Identify the parasite.
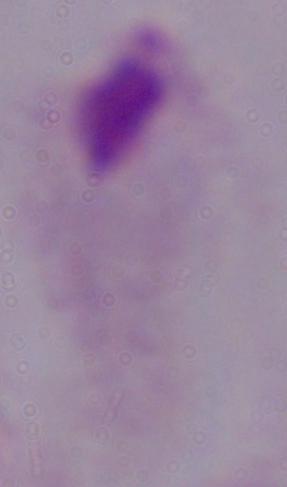

A trichomonad.

Summary:
  - Modality: photomicrograph
  - Magnification: 1000x